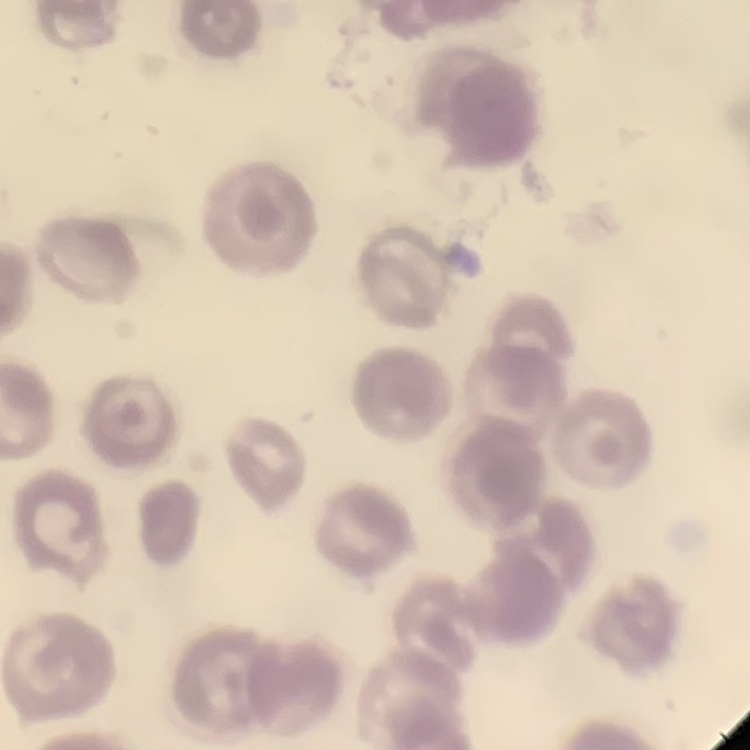

The red blood cells exhibit no rouleaux formation. Thin blood film. Field's or Giemsa stain. One tile cut from a larger photomicrograph.